Locate every blood parasite and identify its species.
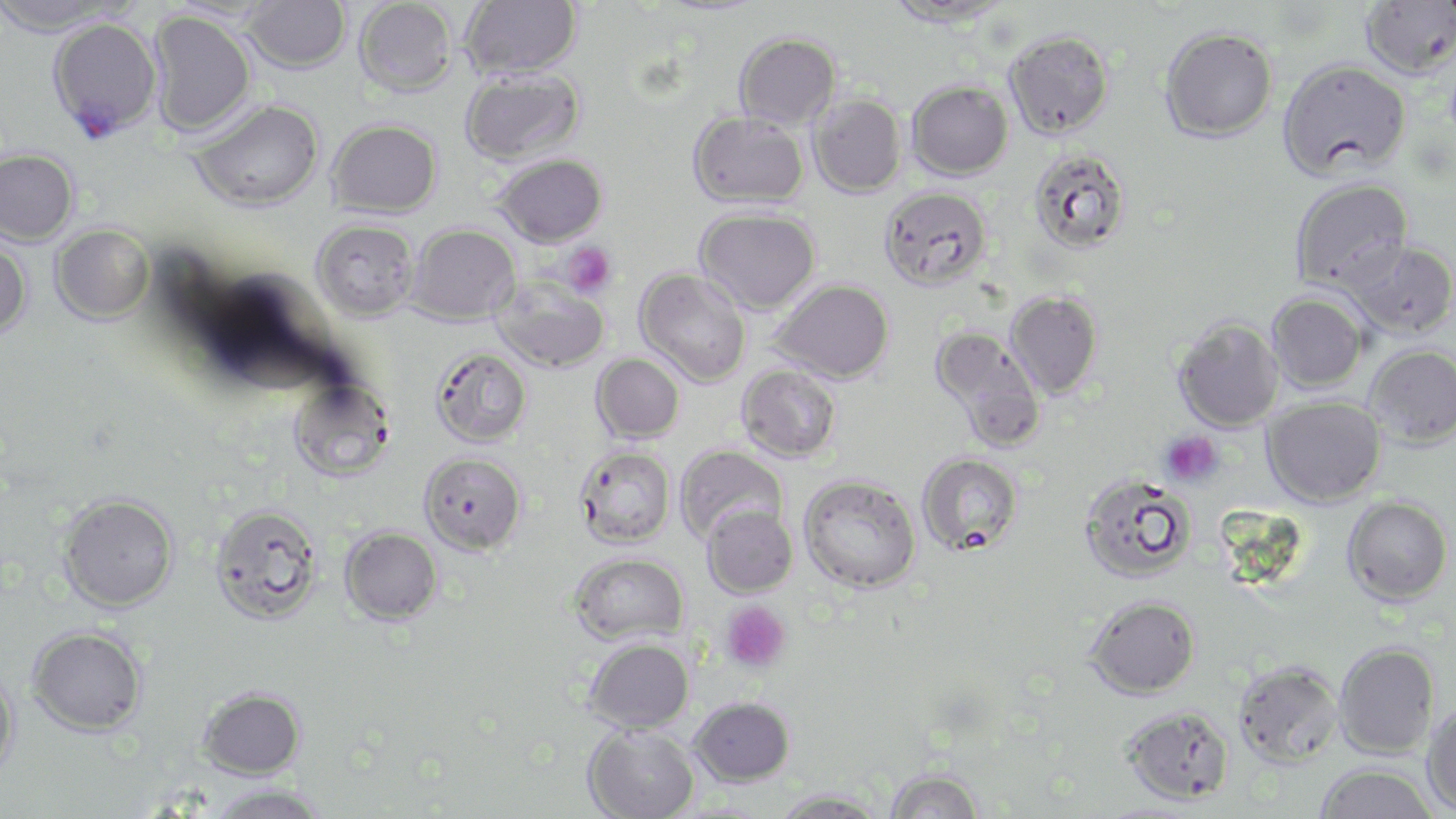
Approximate bounding boxes as [x1, y1, x2, y2] in pixels.
Plasmodium falciparum-infected red blood cells: [48, 17, 162, 140].
No Plasmodium ovale, Plasmodium malariae, Plasmodium vivax, Babesia divergens, or Trypanosoma brucei observed.

Summary:
  - Platelet locations: [560, 242, 618, 296], [1158, 430, 1223, 488], [721, 601, 790, 673]
  - Uninfected red blood cell locations: [0, 0, 124, 35], [355, 0, 457, 96], [460, 0, 582, 80], [882, 0, 1013, 26], [243, 1, 351, 73], [1360, 1, 1456, 80], [148, 10, 255, 138], [1160, 27, 1277, 142], [1006, 30, 1114, 138], [734, 33, 841, 130], [1277, 59, 1411, 180], [460, 68, 585, 166], [907, 80, 1012, 179], [808, 94, 907, 198], [189, 99, 324, 213], [688, 112, 808, 208], [328, 119, 442, 217], [0, 149, 79, 246], [1028, 149, 1132, 255], [493, 154, 607, 247], [1289, 177, 1415, 295], [878, 186, 992, 292], [696, 208, 820, 314], [312, 219, 418, 322], [407, 223, 519, 325], [51, 225, 153, 324], [0, 237, 32, 339], [1344, 241, 1456, 339], [635, 268, 751, 387], [491, 277, 609, 373], [771, 278, 895, 383], [1005, 291, 1102, 398], [1267, 292, 1369, 393], [1173, 318, 1283, 432], [929, 326, 1046, 452], [1365, 344, 1456, 448], [430, 348, 532, 447], [591, 353, 685, 444], [737, 366, 842, 463], [288, 378, 395, 482], [1262, 396, 1386, 507], [574, 445, 676, 548], [674, 445, 787, 546], [419, 452, 526, 555], [917, 453, 1023, 555], [1077, 473, 1196, 584], [798, 475, 921, 593], [57, 493, 179, 613], [1342, 496, 1453, 606], [210, 503, 324, 624], [702, 504, 798, 598], [340, 526, 443, 625], [568, 552, 688, 646], [1085, 595, 1201, 699], [27, 625, 148, 736], [584, 637, 693, 733], [1334, 642, 1440, 759], [1234, 661, 1344, 767], [0, 666, 20, 780], [197, 686, 306, 779], [690, 696, 794, 785], [1422, 701, 1456, 815], [1121, 705, 1235, 805], [583, 725, 699, 819], [1315, 763, 1438, 819], [885, 769, 983, 819], [207, 784, 327, 819], [773, 790, 887, 818]
  - Slide-level diagnosis: Plasmodium falciparum
  - Preparation: thin blood film
  - Modality: optical microscopy
  - Image size: 1456×819 pixels
  - Magnification: 1000x
  - Field of view: single
  - Stain: May-Grünwald-Giemsa